Locate every blood parasite and identify its species.
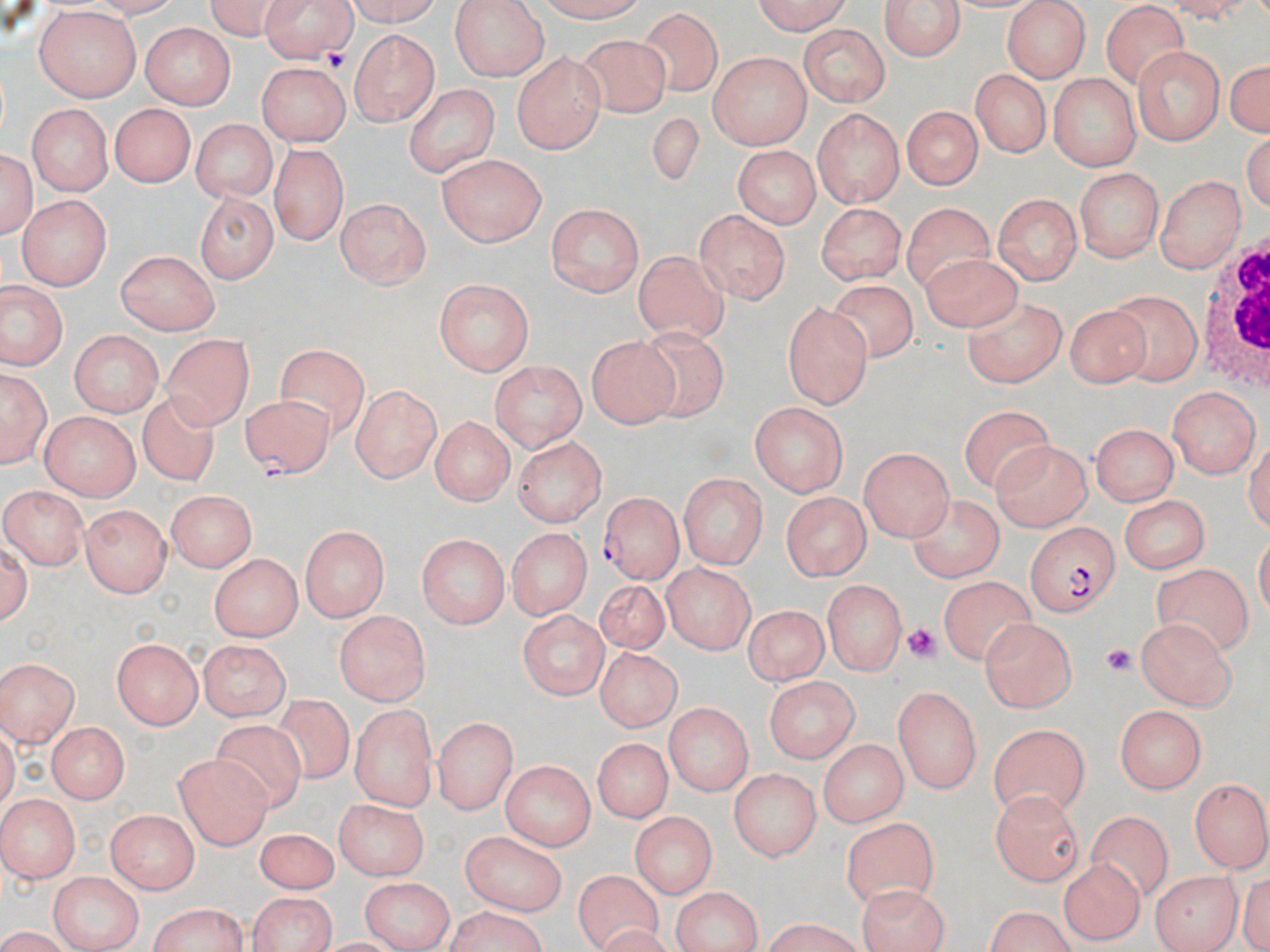
Approximate bounding boxes as (x1, y1, x2, y2) in pixels.
Plasmodium falciparum-infected red blood cells: (241, 393, 333, 479), (599, 495, 682, 584), (1026, 520, 1123, 616).
No Plasmodium ovale, Plasmodium malariae, Plasmodium vivax, Babesia divergens, or Trypanosoma brucei observed.

Summary:
  - Platelet locations: (320, 42, 350, 75), (906, 624, 937, 664), (1102, 643, 1135, 677)
  - White blood cell locations: (1200, 242, 1269, 392)
  - Uninfected red blood cell locations: (200, 0, 287, 35), (259, 0, 359, 72), (338, 0, 447, 26), (449, 0, 547, 78), (536, 0, 656, 23), (745, 0, 853, 33), (881, 0, 966, 64), (1101, 3, 1188, 87), (1002, 4, 1093, 81), (32, 6, 141, 100), (641, 6, 723, 98), (138, 23, 234, 108), (798, 25, 888, 105), (351, 30, 437, 127), (579, 35, 674, 118), (1132, 46, 1228, 143), (511, 53, 604, 153), (710, 53, 811, 148), (1223, 55, 1270, 138), (252, 63, 350, 144), (968, 69, 1051, 156), (1051, 75, 1139, 169), (404, 82, 499, 174), (25, 102, 111, 196), (106, 103, 194, 187), (898, 105, 983, 190), (811, 107, 907, 208), (640, 112, 705, 204), (189, 119, 275, 203), (0, 140, 38, 244), (271, 142, 347, 247), (734, 146, 818, 228), (440, 156, 544, 247), (1073, 166, 1164, 264), (449, 171, 613, 267), (1157, 172, 1247, 270), (194, 190, 278, 285), (992, 193, 1083, 283), (18, 195, 113, 290), (334, 197, 433, 291), (543, 201, 644, 297), (815, 201, 908, 282), (903, 202, 998, 284), (695, 208, 791, 305), (915, 248, 1021, 333), (113, 250, 217, 331), (635, 251, 728, 343), (434, 279, 534, 377), (822, 280, 923, 367), (0, 282, 66, 372), (1107, 288, 1201, 383), (964, 296, 1067, 387), (779, 303, 873, 406), (1064, 306, 1153, 398), (67, 328, 164, 414), (162, 331, 253, 426), (633, 331, 729, 421), (584, 332, 680, 429), (276, 343, 370, 430), (490, 359, 588, 453), (1, 368, 47, 468), (1165, 383, 1259, 476), (349, 384, 442, 484), (137, 389, 218, 488), (746, 401, 849, 495), (955, 406, 1060, 494), (39, 412, 139, 499), (427, 417, 512, 506), (1088, 423, 1178, 507), (512, 436, 605, 524), (992, 439, 1089, 529), (859, 446, 955, 540), (677, 470, 768, 572), (1, 489, 85, 570), (166, 491, 257, 573), (780, 491, 875, 580), (1118, 494, 1210, 573), (909, 496, 1003, 579), (81, 504, 174, 597), (296, 523, 392, 621), (504, 527, 589, 619), (417, 533, 509, 627), (207, 552, 303, 642), (664, 563, 754, 655), (1155, 564, 1254, 656), (938, 575, 1036, 671), (821, 578, 909, 676), (590, 580, 670, 659), (740, 605, 828, 692), (516, 606, 610, 697), (331, 608, 433, 707), (1139, 619, 1233, 709), (982, 620, 1077, 710), (111, 640, 203, 729), (196, 641, 293, 717), (585, 650, 685, 738), (0, 656, 81, 746), (761, 676, 859, 761), (891, 684, 978, 795), (269, 693, 357, 787), (351, 701, 435, 806), (662, 702, 752, 793), (1117, 707, 1209, 793), (433, 716, 518, 813), (43, 721, 133, 801), (211, 723, 307, 815), (988, 723, 1090, 816), (817, 738, 907, 827), (593, 741, 671, 823), (174, 751, 272, 848), (502, 761, 594, 851), (728, 769, 819, 863), (1187, 777, 1270, 871), (989, 787, 1086, 885), (0, 792, 80, 883), (333, 797, 431, 880), (106, 810, 199, 895), (1086, 810, 1172, 897), (629, 811, 719, 897), (840, 816, 939, 907), (253, 827, 338, 891), (455, 829, 568, 914), (1061, 858, 1146, 944), (1151, 868, 1241, 949), (568, 869, 661, 949), (49, 872, 144, 952), (360, 875, 455, 952), (849, 886, 948, 951), (669, 887, 765, 950), (244, 891, 341, 952), (143, 903, 249, 952), (979, 906, 1080, 952), (438, 909, 552, 952)
  - Slide-level diagnosis: Plasmodium falciparum
  - Field of view: single
  - Modality: optical microscopy
  - Stain: May-Grünwald-Giemsa
  - Preparation: thin blood film
  - Image size: 1270×952 pixels
  - Magnification: 1000x